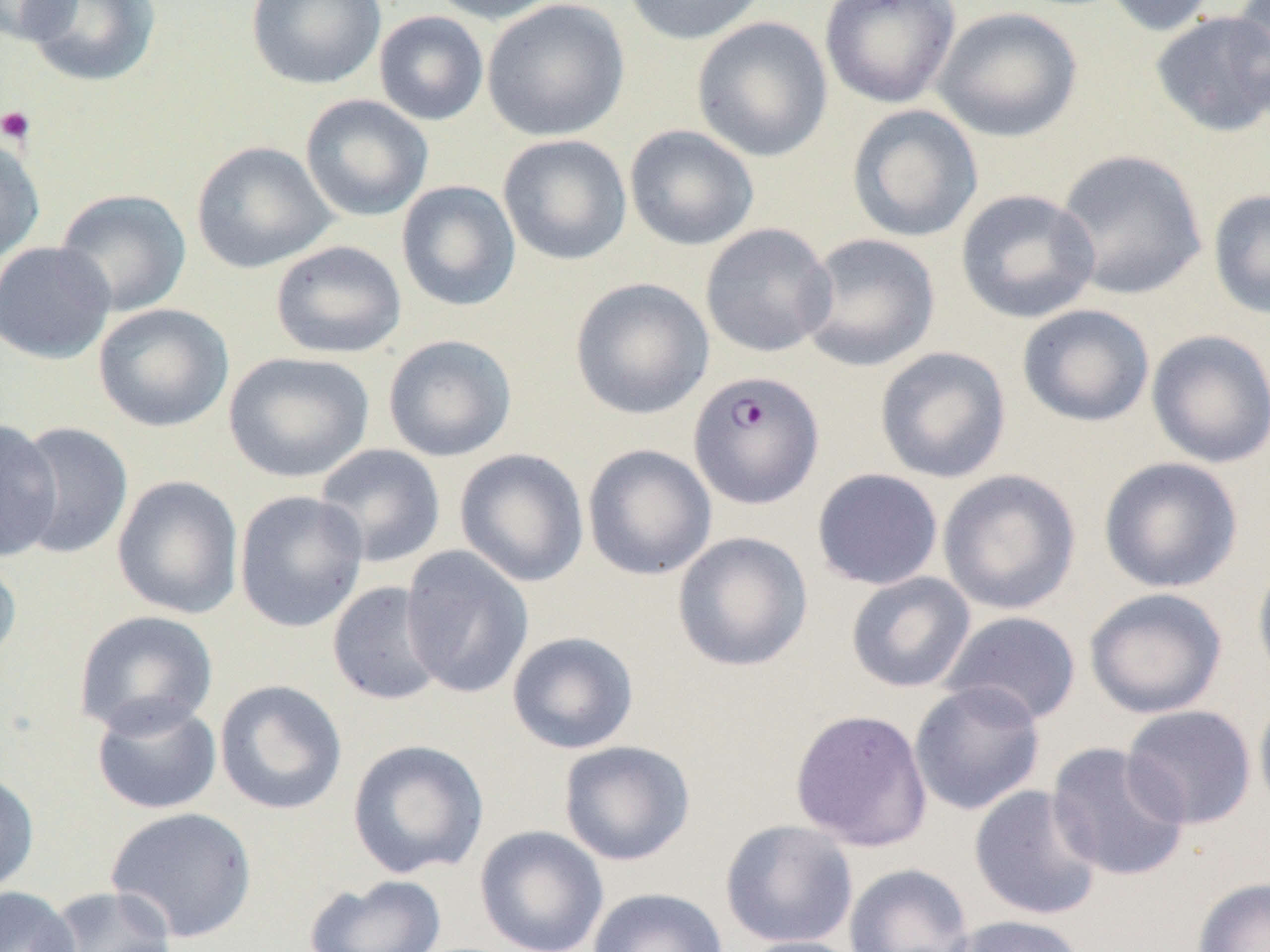

Summary:
  - Coordinate format: approximate bounding boxes as [x1, y1, x2, y2] in pixels
  - Plasmodium falciparum-infected red blood cell locations: [688, 370, 824, 509]
  - Platelet locations: [0, 105, 36, 146]
  - Uninfected red blood cell locations: [0, 0, 77, 44], [21, 0, 162, 88], [246, 0, 387, 90], [426, 0, 566, 25], [482, 0, 630, 142], [622, 0, 768, 45], [819, 0, 961, 108], [1099, 0, 1220, 37], [1226, 0, 1270, 113], [932, 6, 1083, 142], [1150, 9, 1270, 137], [373, 11, 489, 126], [690, 15, 833, 163], [300, 94, 434, 222], [846, 104, 983, 243], [624, 124, 760, 251], [0, 134, 46, 267], [497, 134, 633, 265], [191, 141, 337, 273], [1055, 149, 1208, 300], [396, 180, 521, 312], [54, 188, 192, 318], [955, 189, 1100, 324], [1207, 189, 1270, 319], [700, 223, 837, 358], [798, 232, 941, 373], [270, 240, 407, 359], [0, 241, 115, 364], [569, 277, 715, 420], [93, 303, 234, 433], [1017, 304, 1155, 428], [1146, 329, 1270, 469], [382, 334, 517, 462], [874, 346, 1012, 484], [223, 351, 374, 484], [0, 419, 63, 561], [12, 421, 133, 559], [313, 443, 446, 568], [582, 444, 717, 581], [454, 448, 590, 587], [1098, 456, 1244, 593], [812, 468, 944, 590], [937, 469, 1081, 615], [112, 475, 244, 620], [233, 489, 368, 633], [671, 531, 813, 672], [400, 546, 534, 698], [0, 550, 22, 672], [1251, 552, 1270, 693], [845, 572, 976, 693], [327, 581, 448, 706], [1083, 587, 1228, 719], [73, 610, 220, 737], [939, 611, 1081, 726], [506, 631, 639, 754], [214, 679, 348, 816], [908, 680, 1046, 816], [1254, 689, 1270, 823], [91, 695, 222, 815], [1121, 705, 1257, 829], [789, 709, 933, 851], [347, 739, 489, 878], [558, 740, 696, 866], [1046, 742, 1190, 883], [0, 771, 39, 896], [969, 785, 1104, 921], [105, 806, 258, 943], [720, 819, 858, 949], [474, 825, 609, 952], [843, 862, 975, 952], [304, 873, 447, 952], [1191, 877, 1270, 952], [0, 886, 81, 952], [43, 886, 178, 952], [587, 887, 730, 952], [946, 915, 1088, 952], [736, 936, 869, 952]
  - Slide-level diagnosis: Plasmodium falciparum
  - Image size: 1270×952 pixels
  - Magnification: 1000x
  - Modality: optical microscopy
  - Preparation: thin blood film
  - Field of view: one of a larger specimen